Report the malaria status of this cell.
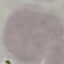
Uninfected.

preparation = thin blood film
capture = smartphone camera at the microscope eyepiece
image type = cell patch, automatically extracted from a larger field of view and resized to 64 × 64 pixels
stain = Giemsa